Classify this cell by malaria status.
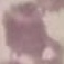

Uninfected.

preparation = thin blood film
stain = Giemsa
capture = smartphone through the microscope eyepiece
image type = automatically extracted cell patch, resized to 64 × 64 pixels